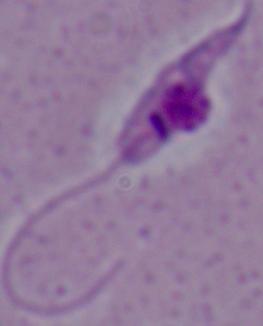 1000x magnification. Micrograph. A Leishmania parasite is shown.